Locate every malaria parasite.
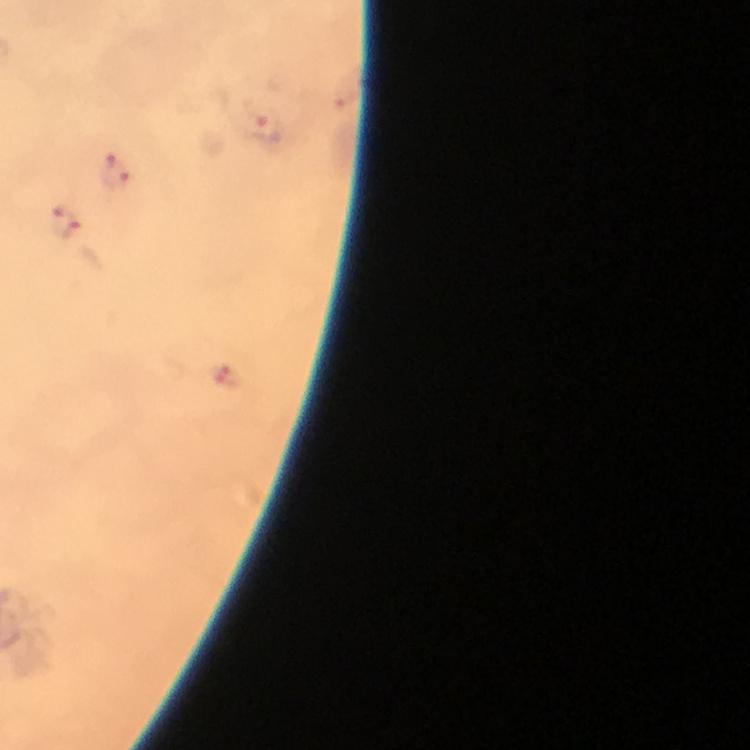

Approximate centers as {x, y} in pixels.
Malaria parasites: {268, 129}, {116, 171}, {63, 222}, {226, 375}.

capture = smartphone camera through the microscope
stain = Giemsa
context = from a diagnostic examination for malaria
image size = 750×750 pixels
preparation = thick blood film
immersion oil = applied
cropped from = one field of view
magnification = 100x